Outline each blood parasite and name the species.
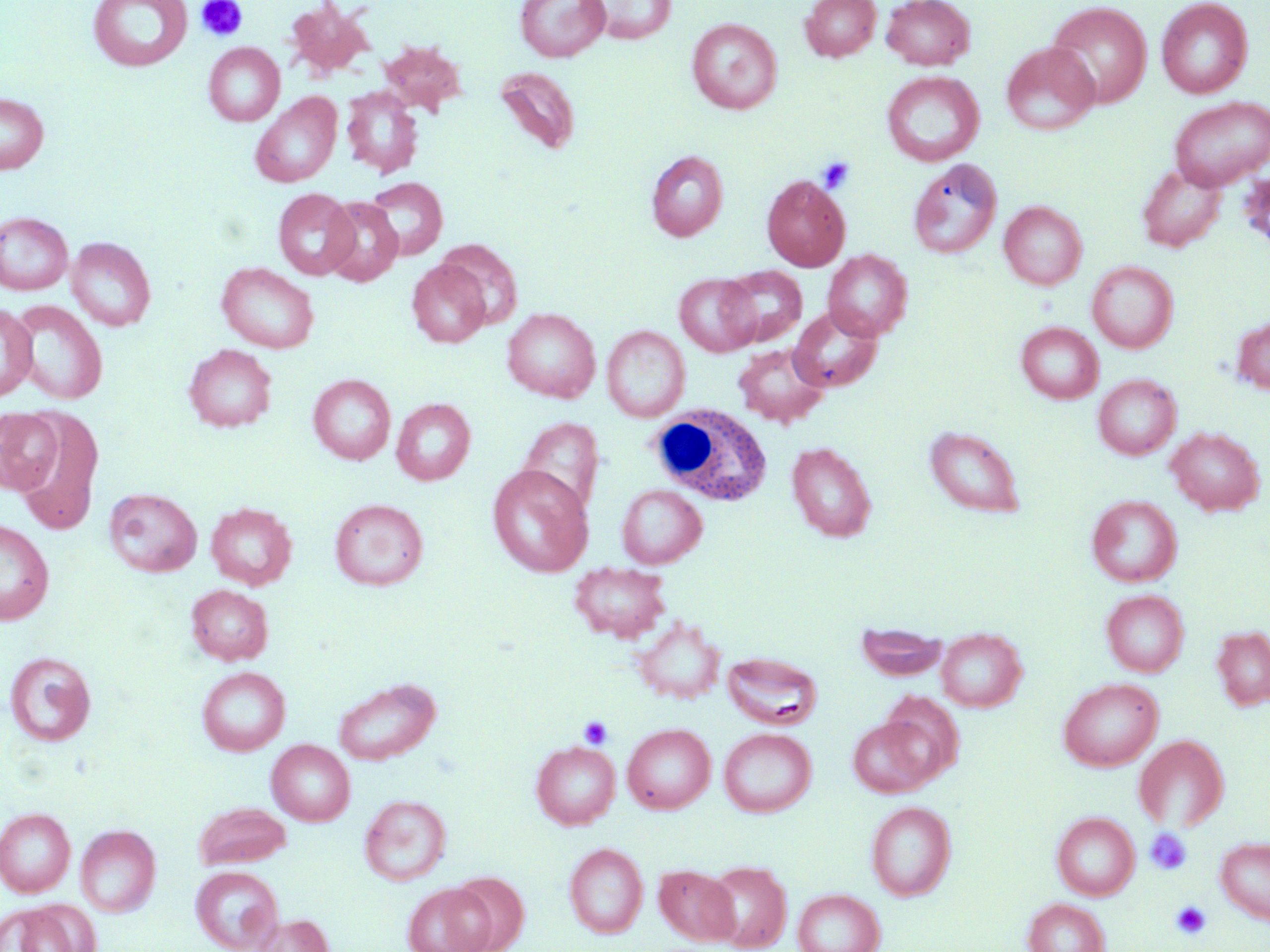
No blood parasites observed.

Approximate bounding boxes as [x1, y1, x2, y2] in pixels. White blood cell locations: [647, 405, 773, 506]. Platelet locations: [195, 0, 248, 42], [817, 155, 856, 194], [578, 715, 613, 749], [1145, 828, 1192, 875], [1171, 901, 1211, 941]. Uninfected red blood cell locations: [88, 0, 192, 72], [515, 0, 609, 62], [589, 0, 676, 44], [801, 0, 881, 61], [882, 0, 975, 70], [1156, 0, 1253, 98], [284, 1, 376, 80], [1047, 2, 1152, 108], [687, 18, 782, 114], [378, 39, 468, 115], [203, 42, 285, 126], [1001, 42, 1099, 135], [495, 67, 580, 154], [882, 71, 984, 167], [341, 87, 423, 178], [0, 92, 49, 175], [251, 92, 342, 188], [1169, 96, 1270, 190], [646, 149, 728, 241], [908, 158, 1002, 259], [1137, 164, 1226, 252], [761, 174, 850, 271], [364, 177, 447, 260], [273, 188, 358, 280], [321, 196, 403, 287], [999, 201, 1087, 290], [0, 212, 73, 295], [66, 237, 156, 331], [436, 239, 523, 330], [822, 249, 913, 341], [1087, 261, 1178, 353], [216, 262, 320, 353], [407, 262, 491, 348], [720, 266, 807, 347], [674, 273, 760, 357], [8, 300, 109, 405], [0, 303, 37, 403], [788, 307, 883, 392], [502, 308, 600, 402], [1232, 316, 1270, 395], [1016, 321, 1104, 403], [602, 325, 690, 421], [733, 343, 828, 427], [184, 344, 277, 432], [308, 374, 396, 465], [1093, 374, 1180, 460], [392, 398, 476, 485], [12, 408, 104, 536], [0, 409, 63, 494], [518, 417, 604, 515], [925, 425, 1025, 517], [1166, 426, 1265, 515], [786, 441, 877, 542], [487, 465, 593, 577], [616, 484, 706, 568], [104, 488, 202, 577], [1087, 495, 1182, 587], [329, 498, 429, 591], [206, 503, 297, 589], [0, 520, 54, 625], [570, 563, 671, 643], [185, 584, 273, 665], [1101, 589, 1189, 677], [632, 616, 725, 704], [1213, 626, 1270, 710], [935, 627, 1027, 712], [4, 651, 97, 747], [722, 652, 823, 729], [196, 667, 290, 756], [333, 676, 441, 765], [1058, 677, 1163, 771], [879, 691, 964, 781], [848, 718, 937, 798], [622, 723, 715, 814], [718, 727, 816, 817], [1133, 734, 1230, 831], [266, 740, 354, 825], [531, 741, 620, 829], [360, 794, 451, 885], [194, 801, 291, 869], [866, 801, 956, 901], [0, 808, 75, 896], [1052, 812, 1139, 900], [75, 825, 161, 916], [1216, 836, 1270, 925], [565, 842, 648, 939], [704, 861, 792, 951], [655, 864, 740, 945], [190, 866, 282, 952], [450, 871, 528, 952], [403, 882, 492, 952], [794, 888, 885, 952], [1023, 898, 1109, 952], [1, 902, 94, 952], [252, 914, 333, 952]. Slide-level diagnosis: no evidence of blood parasites. Thin blood smear. Optical microscopy. Image is 1270×952 pixels. Single field of view. May-Grünwald-Giemsa-stained preparation. Captured at 1000x magnification.